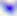
Micrograph. Captured at 400x magnification. Toxoplasma gondii is seen.